Classify this cell by malaria status.
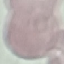
Uninfected.

{
  "preparation": "thin blood smear",
  "stain": "Giemsa",
  "image_type": "automatically extracted cell patch, resized to 64 × 64 pixels",
  "capture": "smartphone camera at the microscope eyepiece"
}